Assess the morphology of the red blood cells.
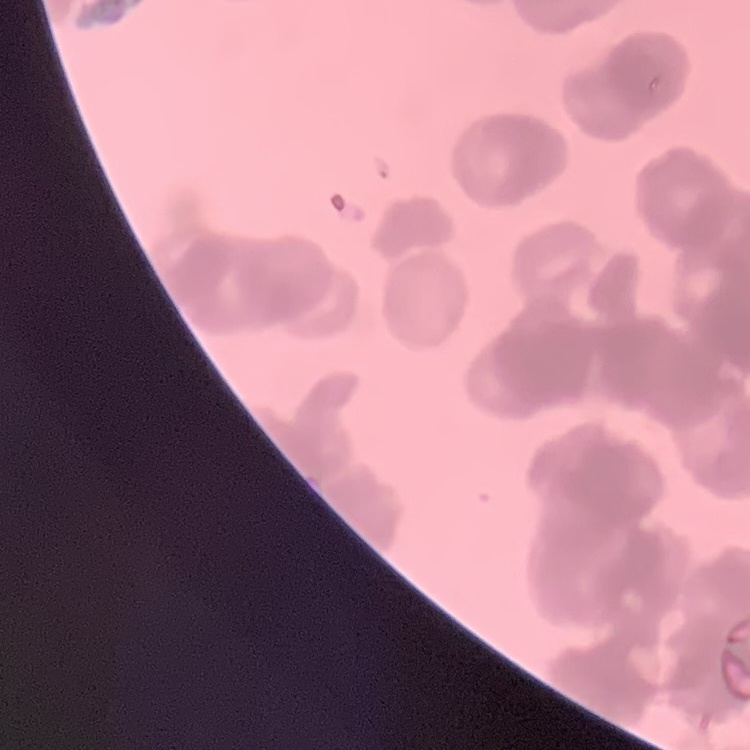
Rouleaux formation.

Stained with either Field's or Giemsa. Thin blood film. One tile cut from a larger photomicrograph.